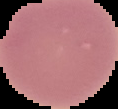

Summary:
  - Image type: segmented cell region on a black background
  - Result: negative for Plasmodium parasites
  - Image size: 118×109 pixels
  - Preparation: thin blood film